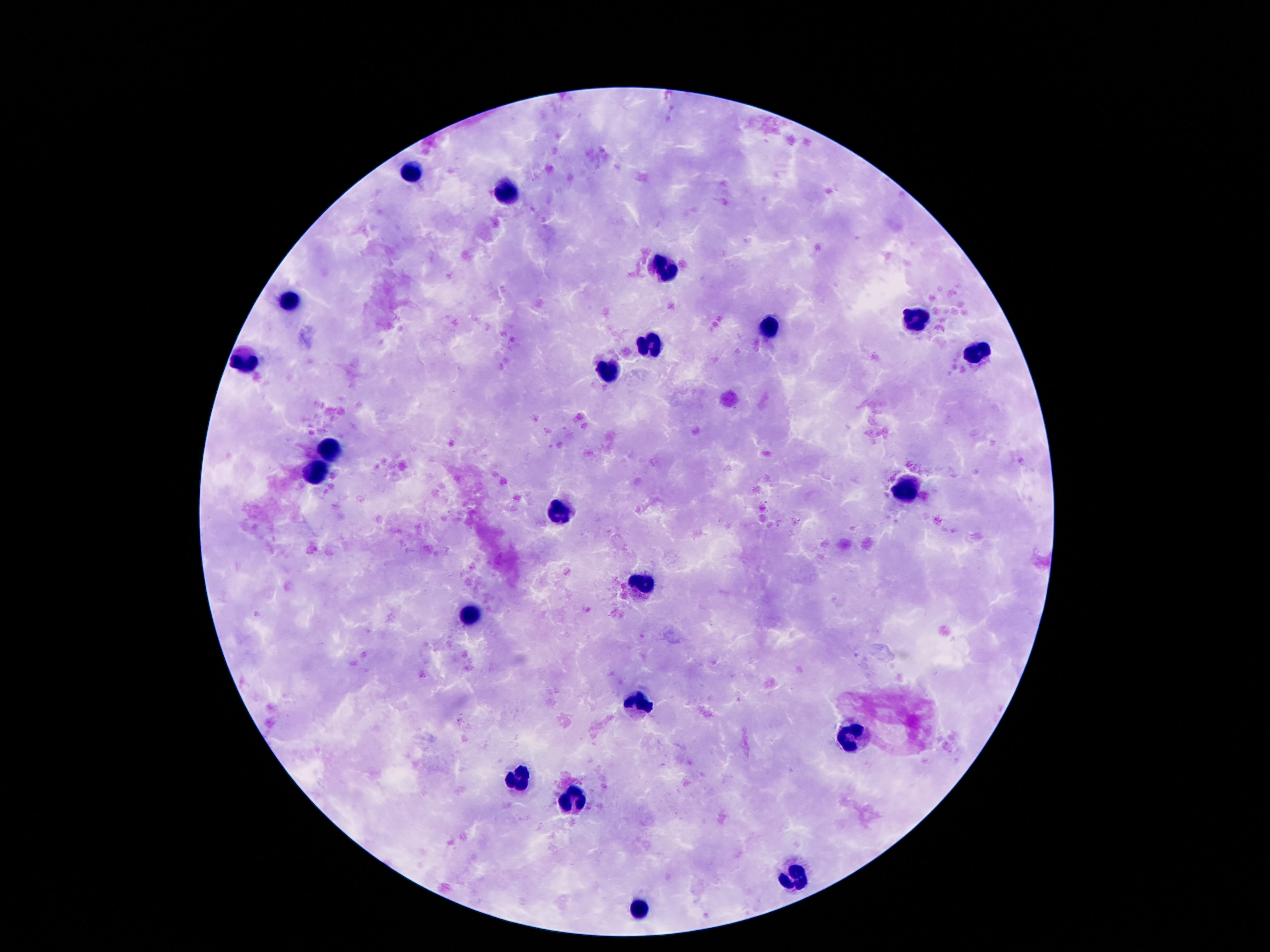
Approximate centers as {x, y} in pixels.
Summary:
  - Leukocyte locations: {407, 173}, {505, 195}, {666, 270}, {288, 301}, {913, 322}, {766, 328}, {647, 345}, {976, 354}, {246, 364}, {605, 372}, {327, 448}, {318, 473}, {908, 492}, {556, 513}, {638, 580}, {467, 613}, {638, 702}, {845, 736}, {512, 783}, {572, 804}, {794, 874}, {642, 906}
  - Patient malaria status: uninfected
  - Magnification: 100x
  - Image size: 1270×952 pixels
  - Field of view: one from this slide
  - Stain: Giemsa
  - Capture: smartphone camera through the microscope eyepiece
  - Preparation: thick blood film